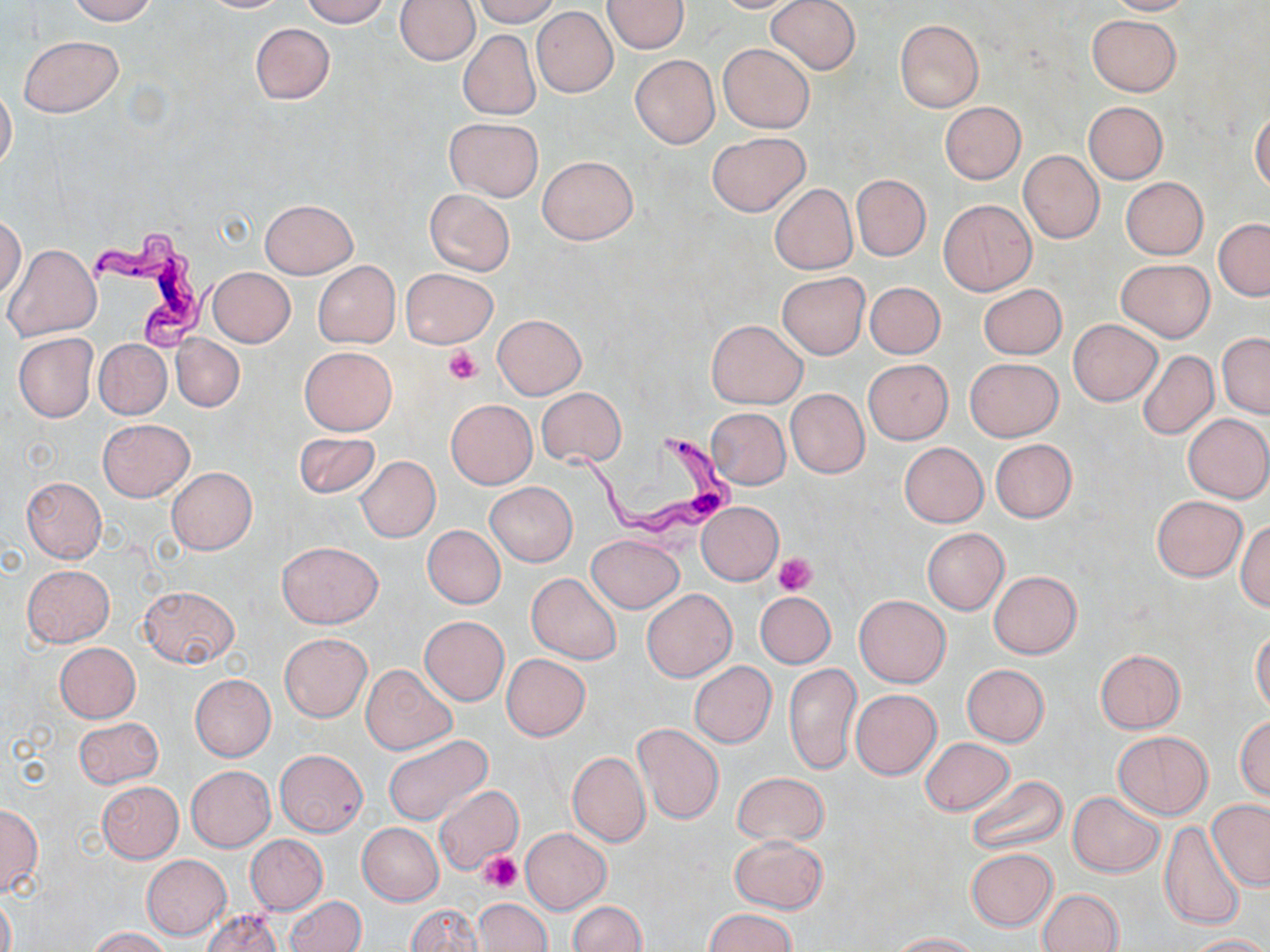

slide-level diagnosis = Trypanosoma brucei
image size = 1270×952 pixels
stain = May-Grünwald-Giemsa
Trypanosoma brucei locations = approximate bounding boxes as (x1,y1)-(x2,y2) corner pairs in pixels: (87,227)-(221,352), (559,428)-(743,542)
modality = optical microscopy
uninfected red blood cell locations = approximate bounding boxes as (x1,y1)-(x2,y2) corner pairs in pixels: (68,0)-(156,25), (197,0)-(292,13), (301,0)-(389,26), (472,0)-(560,25), (603,0)-(690,53), (709,0)-(806,13), (767,0)-(860,74), (1102,0)-(1195,16), (394,1)-(480,66), (531,6)-(618,97), (1086,14)-(1181,96), (895,19)-(983,114), (250,23)-(334,104), (458,30)-(541,120), (19,36)-(123,116), (718,42)-(815,133), (630,54)-(720,149), (0,82)-(17,172), (1083,101)-(1168,184), (941,102)-(1026,183), (1251,110)-(1270,193), (445,118)-(543,200), (708,132)-(809,216), (1018,150)-(1104,243), (538,155)-(638,246), (850,174)-(931,261), (1119,176)-(1208,259), (770,183)-(857,274), (424,188)-(515,276), (258,199)-(357,279), (938,199)-(1037,296), (0,215)-(26,298), (1214,218)-(1270,300), (4,244)-(101,341), (1116,259)-(1214,342), (313,261)-(400,348), (207,267)-(295,347), (400,268)-(498,348), (776,272)-(869,359), (865,281)-(944,359), (977,283)-(1067,360), (492,314)-(587,399), (706,319)-(807,408), (1069,320)-(1161,405), (1218,332)-(1270,418), (13,333)-(98,422), (172,334)-(244,411), (95,339)-(171,418), (299,346)-(396,436), (1138,350)-(1218,438), (965,358)-(1063,441), (863,359)-(952,444), (536,387)-(627,466), (785,388)-(869,479), (446,400)-(537,488), (707,408)-(791,488), (1183,413)-(1270,503), (98,419)-(194,501), (293,431)-(381,499), (990,439)-(1076,521), (899,442)-(988,526), (356,456)-(440,542), (166,468)-(256,553), (22,477)-(106,561), (484,482)-(578,567), (1151,496)-(1247,581), (697,502)-(783,584), (1236,520)-(1270,610), (423,525)-(506,608), (923,528)-(1008,614), (587,534)-(684,612), (277,541)-(383,628), (23,564)-(114,647), (989,571)-(1081,658), (527,573)-(621,664), (138,585)-(240,670), (641,588)-(737,682), (755,591)-(836,668), (855,595)-(950,687), (420,616)-(509,706), (1251,629)-(1270,716), (280,632)-(371,721), (55,643)-(140,722), (1095,650)-(1185,732), (501,654)-(590,740), (690,662)-(776,746), (785,663)-(862,775), (961,663)-(1049,745), (360,664)-(455,755), (191,674)-(276,761), (851,689)-(941,779), (1235,715)-(1270,799), (72,716)-(163,788), (633,722)-(723,824), (1113,731)-(1212,818), (382,734)-(495,829), (920,738)-(1014,815), (275,750)-(368,836), (567,750)-(650,847), (185,765)-(276,852), (733,772)-(828,846), (965,774)-(1067,857), (96,781)-(183,863), (434,783)-(525,876), (1068,791)-(1163,878), (1206,800)-(1270,891), (0,804)-(42,896), (358,822)-(444,905), (1160,822)-(1244,931), (521,828)-(610,913), (245,834)-(327,914), (730,835)-(828,913), (966,848)-(1058,930), (141,854)-(231,939), (1038,889)-(1124,952), (1,892)-(15,952), (285,896)-(365,952), (474,898)-(550,951), (567,900)-(647,952), (405,903)-(484,952), (201,908)-(282,951), (704,908)-(797,952), (91,927)-(170,952), (886,932)-(981,951), (1184,935)-(1267,952)
field of view = one of a larger specimen
magnification = 1000x
preparation = thin blood smear
platelet locations = approximate bounding boxes as (x1,y1)-(x2,y2) corner pairs in pixels: (445,345)-(482,385), (774,553)-(817,595), (480,851)-(523,892)